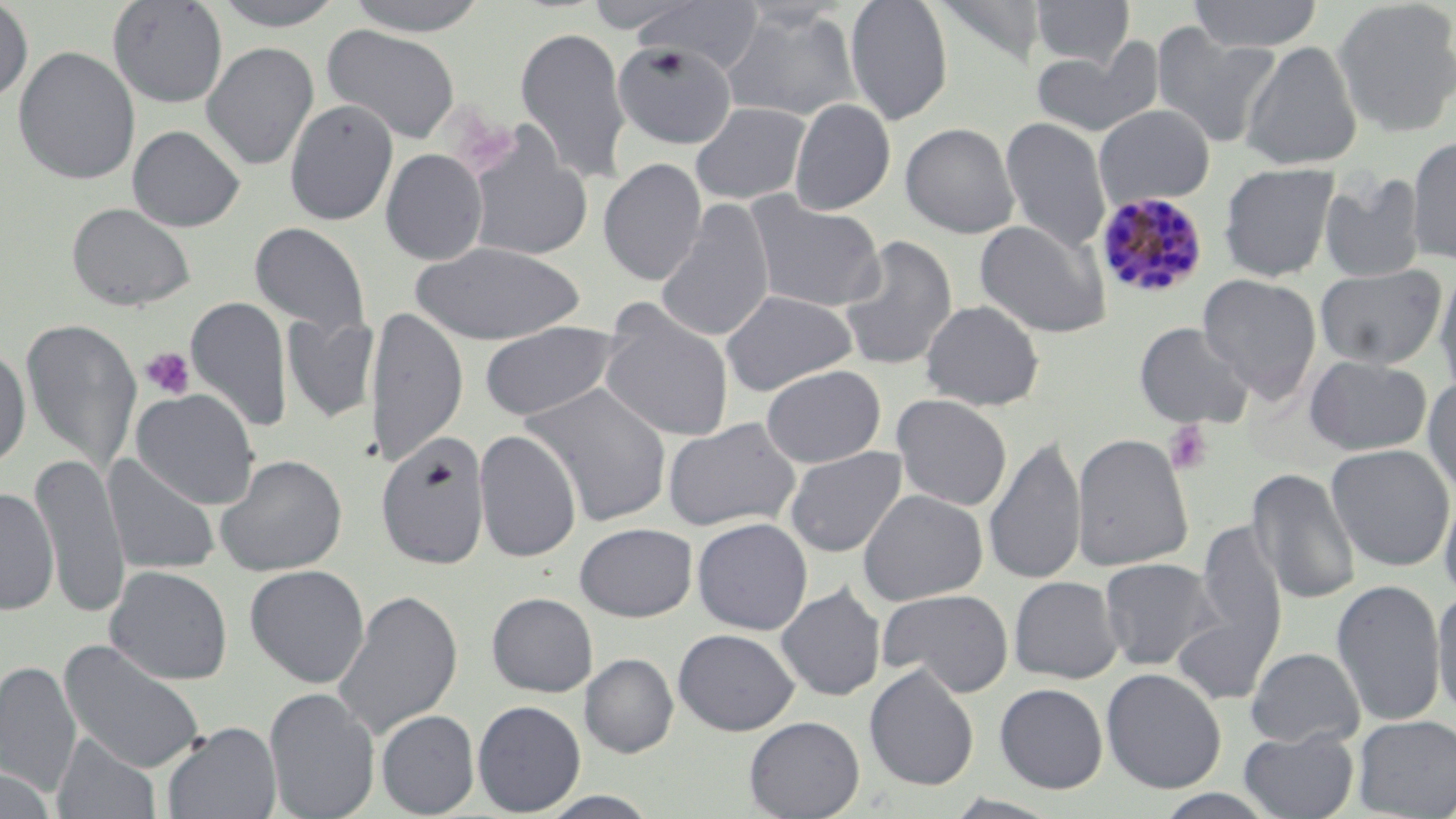

Summary:
  - Coordinate format: approximate bounding boxes as (x1,y1)-(x2,y2) corner pairs in pixels
  - Platelet locations: (139,347)-(195,401), (1164,421)-(1213,476)
  - Plasmodium malariae-infected red blood cell locations: (1095,191)-(1209,299)
  - Uninfected red blood cell locations: (107,0)-(229,109), (206,0)-(351,31), (342,0)-(493,36), (631,0)-(765,74), (845,0)-(953,126), (1030,0)-(1135,68), (1187,0)-(1325,52), (0,1)-(34,104), (933,1)-(1047,68), (1332,1)-(1456,138), (719,7)-(862,123), (322,24)-(461,145), (1151,24)-(1281,147), (515,25)-(631,183), (201,38)-(459,159), (1032,40)-(1165,139), (1240,40)-(1364,170), (201,41)-(320,171), (612,41)-(738,150), (13,45)-(141,186), (284,99)-(398,226), (789,99)-(896,215), (690,102)-(811,204), (1094,104)-(1215,208), (790,109)-(1019,223), (999,116)-(1111,255), (900,122)-(1020,238), (127,125)-(246,232), (464,131)-(594,261), (1407,134)-(1456,265), (380,149)-(488,265), (598,158)-(707,287), (1219,163)-(1339,282), (1318,174)-(1427,283), (745,193)-(886,312), (656,200)-(775,344), (66,202)-(196,312), (975,218)-(1112,339), (249,222)-(370,340), (838,234)-(958,372), (408,241)-(586,345), (1314,265)-(1446,370), (1434,265)-(1456,399), (1197,273)-(1322,400), (720,289)-(857,396), (186,297)-(292,434), (920,300)-(1045,410), (366,305)-(468,468), (599,308)-(735,443), (282,314)-(380,424), (21,318)-(142,474), (478,321)-(624,422), (1134,321)-(1255,429), (0,345)-(31,470), (1304,355)-(1432,455), (761,365)-(886,468), (1423,375)-(1456,499), (520,381)-(673,527), (131,388)-(261,509), (891,394)-(1012,512), (663,417)-(802,532), (474,429)-(582,563), (1071,432)-(1194,571), (375,434)-(490,570), (983,435)-(1087,587), (1325,443)-(1456,572), (785,446)-(908,558), (31,452)-(130,620), (102,454)-(221,576), (215,454)-(347,577), (1247,468)-(1361,605), (1438,484)-(1456,603), (0,488)-(59,616), (857,488)-(988,605), (692,517)-(813,635), (1194,520)-(1288,658), (574,522)-(698,622), (1099,557)-(1220,671), (244,564)-(370,688), (105,565)-(233,686), (1009,576)-(1124,684), (1332,577)-(1446,727), (776,583)-(886,701), (1432,587)-(1456,721), (333,588)-(463,742), (877,588)-(1014,698), (486,592)-(598,697), (1171,604)-(1282,708), (673,628)-(799,735), (58,639)-(207,774), (1245,647)-(1364,748), (580,653)-(678,758), (0,660)-(81,798), (865,664)-(980,791), (1101,667)-(1226,794), (994,683)-(1108,793), (264,687)-(380,819), (473,700)-(586,815), (376,710)-(480,817), (1353,714)-(1456,818), (744,716)-(865,819), (162,722)-(282,819), (1239,729)-(1359,818), (52,734)-(162,819), (0,768)-(57,818), (1152,789)-(1282,819), (534,791)-(663,819), (941,793)-(1066,819)
  - Slide-level diagnosis: Plasmodium malariae
  - Field of view: one of a larger specimen
  - Stain: May-Grünwald-Giemsa
  - Preparation: thin blood film
  - Modality: optical microscopy
  - Magnification: 1000x
  - Image size: 1456×819 pixels